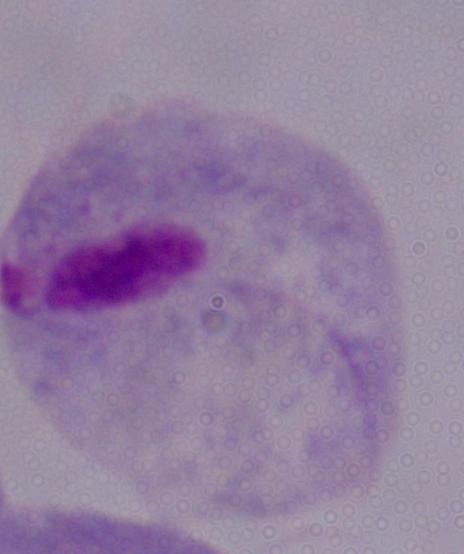

A trichomonad is seen. 1000x magnification. Photomicrograph.